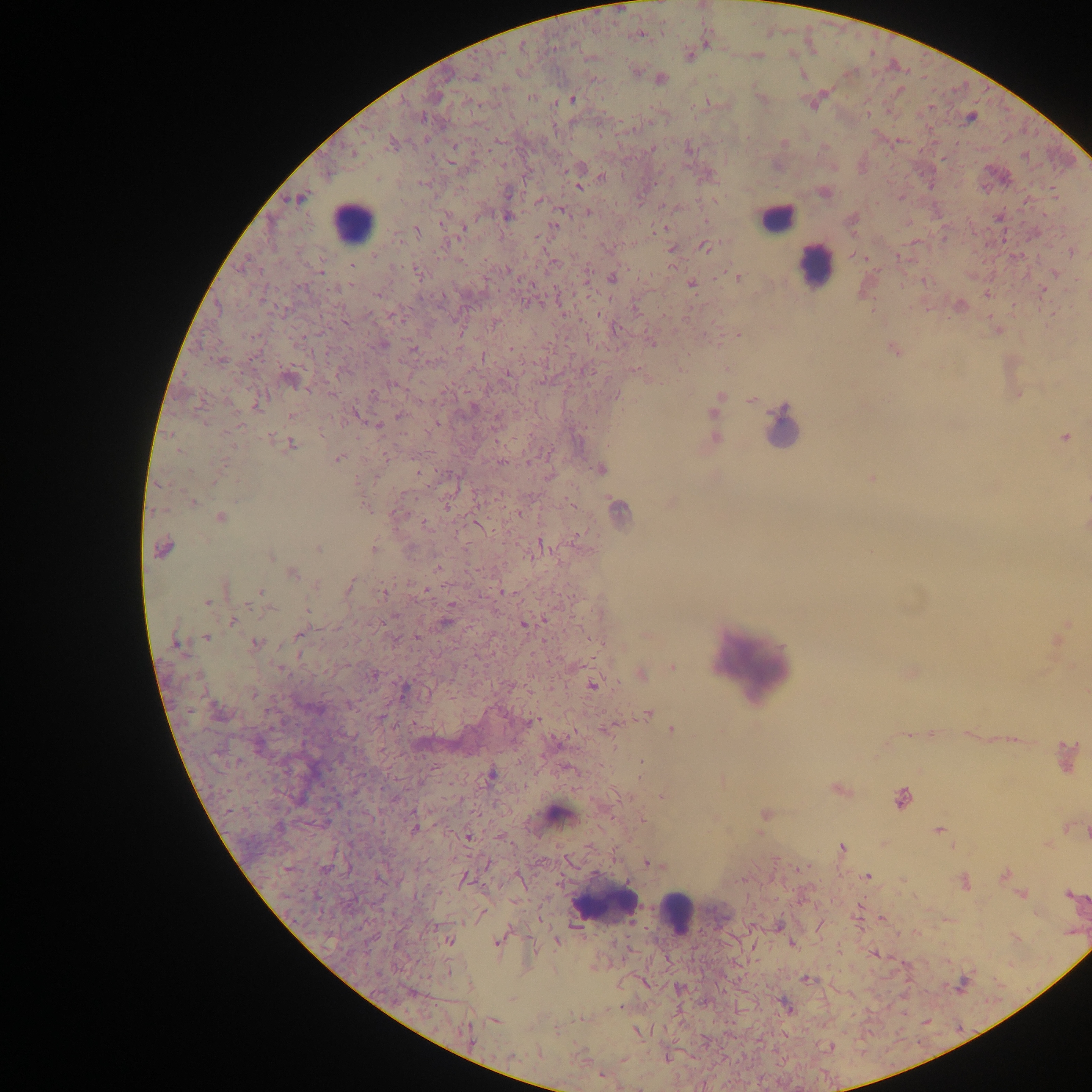

Approximate centers as x y in pixels.
Summary:
  - Leukocyte locations: 776 219; 352 222; 815 265; 782 428; 751 663; 558 816; 605 900; 675 912
  - Malaria parasite locations: 639 34; 706 41; 521 46; 690 55; 756 55; 636 72; 802 74; 474 76; 660 78; 531 97; 761 98; 572 99; 814 100; 707 103; 971 117; 898 142; 783 143; 651 148; 687 148; 327 174; 602 178; 579 186; 823 192; 298 198; 539 201; 560 209; 588 212; 507 216; 444 217; 851 221; 553 226; 664 228; 464 229; 417 230; 703 246; 671 249; 1072 251; 863 258; 352 266; 320 270; 508 270; 1054 273; 737 276; 611 277; 923 281; 691 284; 1043 290; 987 293; 377 294; 958 305; 393 315; 615 328; 997 330; 738 334; 651 342; 381 344; 412 349; 893 349; 679 370; 290 378; 331 393; 1017 393; 616 395; 720 396; 751 400; 258 402; 355 413; 715 413; 399 415; 291 416; 437 424; 378 425; 1063 437; 270 438; 714 438; 290 444; 548 453; 338 457; 501 461; 601 468; 418 472; 871 478; 191 502; 671 502; 365 507; 617 511; 519 512; 220 517; 425 523; 477 523; 1085 525; 541 545; 162 548; 319 549; 374 549; 269 555; 438 567; 292 573; 349 586; 225 587; 425 590; 259 591; 384 592; 208 601; 447 619; 232 620; 523 624; 299 633; 1059 635; 205 636; 178 643; 255 643; 673 666; 910 672; 641 673; 373 674; 591 684; 648 713; 534 721; 609 726; 671 729; 931 733; 966 733; 909 734; 917 734; 1011 739; 258 745; 1066 757; 491 775; 839 789; 662 796; 901 799; 764 815; 642 820; 415 827; 937 830; 467 836; 842 848; 649 862; 1003 874; 866 876; 463 878; 965 882; 1021 894; 1068 894; 882 918; 777 925; 449 940; 557 940; 498 941; 791 944; 874 953; 805 979; 411 993; 787 1007; 494 1021; 637 1031; 468 1035; 623 1059; 601 1074
  - Image size: 1092×1092 pixels
  - Country: Ghana
  - Preparation: thick blood smear
  - Field of view: single
  - Capture: mobile-phone photograph through a microscope